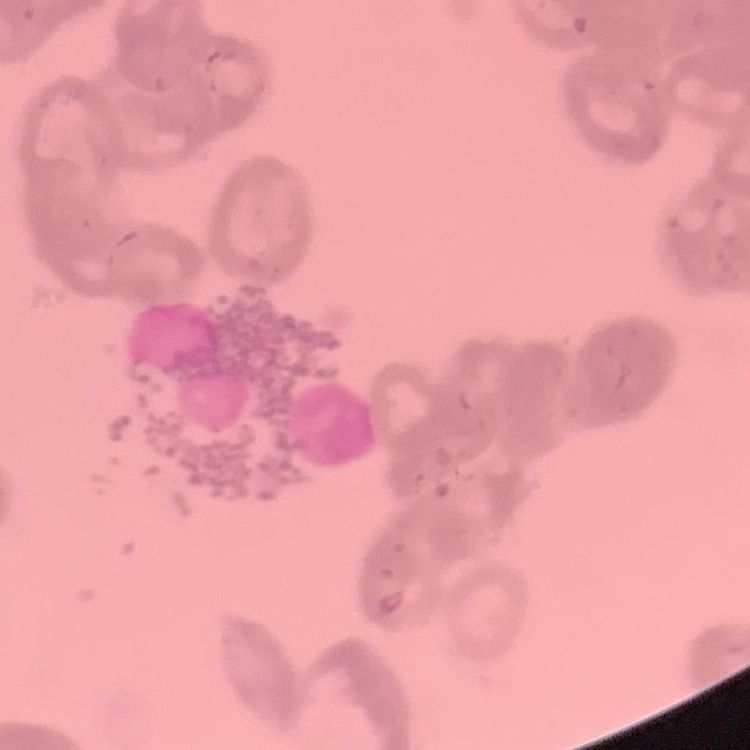
Summary:
  - Red blood cell morphology: rouleaux formation
  - Preparation: thin blood smear
  - Stain: Field's or Giemsa
  - Image type: square crop of a larger photomicrograph